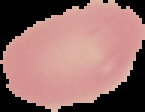

From a thin blood film. Image is 145×112 pixels. Malaria status: uninfected. The area outside the segmented cell region is set to black.